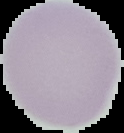

From a thin blood film. The area outside the segmented cell region is set to black. Image is 124×133 pixels. Malaria status: uninfected.